Outline each blood parasite and name the species.
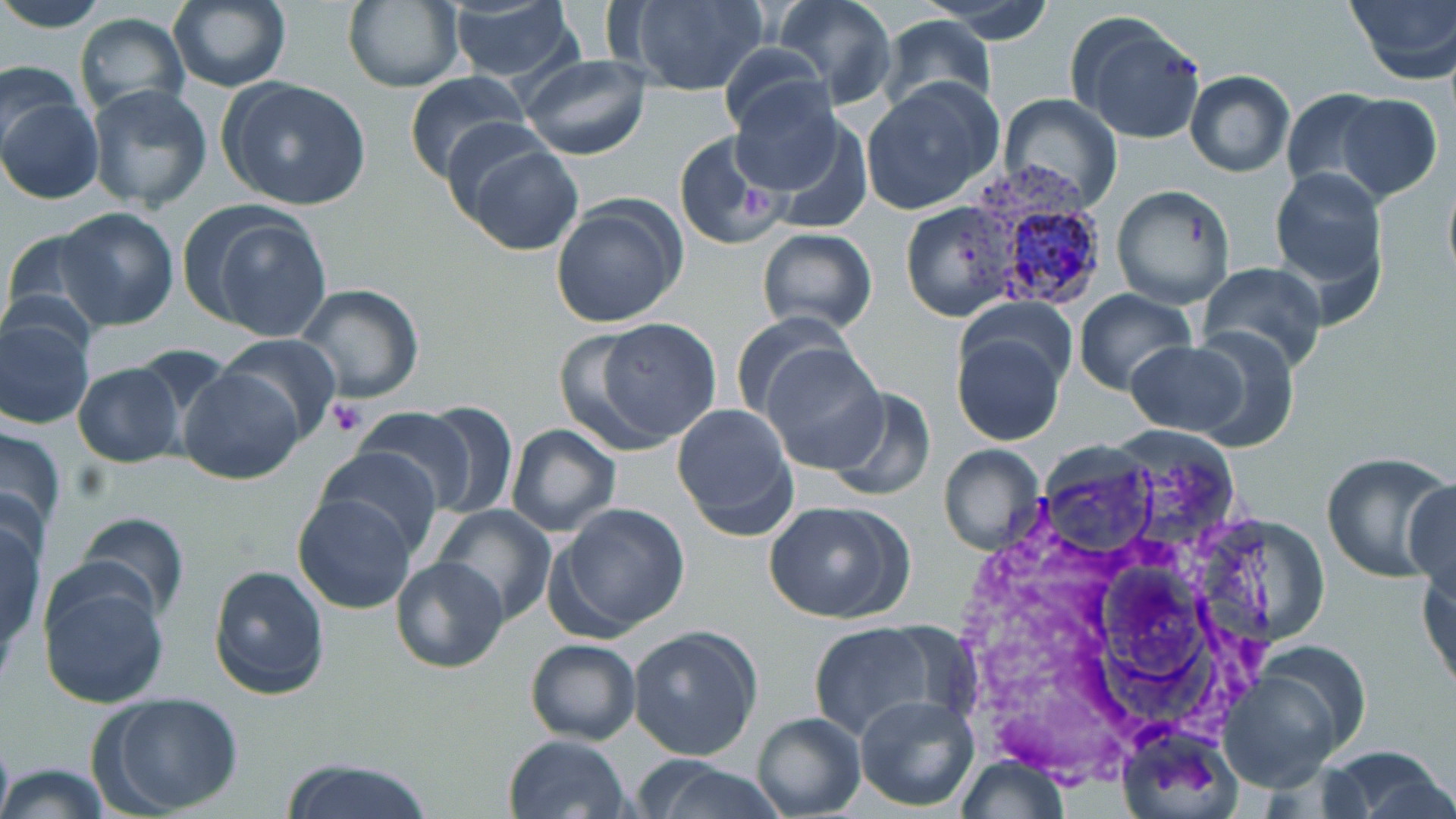
Approximate bounding boxes as named x1/y1/x2/y2 corners in pixels.
Plasmodium vivax-infected red blood cells: (x1=955, y1=162, x2=1109, y2=317).
No Plasmodium falciparum, Plasmodium ovale, Plasmodium malariae, Babesia divergens, or Trypanosoma brucei observed.

slide-level diagnosis = Plasmodium vivax
stain = May-Grünwald-Giemsa
magnification = 1000x
uninfected red blood cell locations = approximate bounding boxes as named x1/y1/x2/y2 corners in pixels: (x1=0, y1=0, x2=110, y2=31), (x1=341, y1=0, x2=465, y2=92), (x1=621, y1=0, x2=768, y2=96), (x1=772, y1=0, x2=896, y2=111), (x1=922, y1=0, x2=1058, y2=44), (x1=1344, y1=0, x2=1456, y2=87), (x1=168, y1=1, x2=290, y2=93), (x1=446, y1=3, x2=582, y2=89), (x1=74, y1=11, x2=190, y2=116), (x1=1068, y1=13, x2=1206, y2=144), (x1=878, y1=14, x2=997, y2=113), (x1=718, y1=40, x2=829, y2=139), (x1=518, y1=53, x2=653, y2=161), (x1=0, y1=61, x2=84, y2=156), (x1=1186, y1=69, x2=1295, y2=177), (x1=403, y1=72, x2=534, y2=186), (x1=220, y1=77, x2=374, y2=213), (x1=864, y1=79, x2=1005, y2=215), (x1=728, y1=80, x2=852, y2=201), (x1=85, y1=83, x2=215, y2=213), (x1=1281, y1=87, x2=1390, y2=194), (x1=998, y1=93, x2=1124, y2=212), (x1=1337, y1=93, x2=1442, y2=202), (x1=2, y1=94, x2=103, y2=206), (x1=675, y1=132, x2=787, y2=253), (x1=458, y1=138, x2=584, y2=257), (x1=1269, y1=167, x2=1388, y2=297), (x1=1441, y1=168, x2=1456, y2=292), (x1=1109, y1=185, x2=1235, y2=309), (x1=551, y1=196, x2=686, y2=329), (x1=899, y1=201, x2=1022, y2=322), (x1=189, y1=205, x2=333, y2=343), (x1=57, y1=206, x2=179, y2=331), (x1=755, y1=227, x2=878, y2=335), (x1=3, y1=228, x2=112, y2=337), (x1=1196, y1=263, x2=1328, y2=376), (x1=293, y1=283, x2=425, y2=404), (x1=1075, y1=289, x2=1198, y2=396), (x1=728, y1=311, x2=856, y2=425), (x1=1, y1=313, x2=95, y2=429), (x1=585, y1=318, x2=724, y2=446), (x1=951, y1=324, x2=1069, y2=447), (x1=1183, y1=328, x2=1301, y2=452), (x1=216, y1=334, x2=343, y2=447), (x1=1123, y1=341, x2=1247, y2=435), (x1=761, y1=343, x2=889, y2=473), (x1=73, y1=363, x2=184, y2=467), (x1=177, y1=364, x2=308, y2=485), (x1=821, y1=386, x2=936, y2=501), (x1=416, y1=401, x2=518, y2=520), (x1=670, y1=401, x2=800, y2=540), (x1=353, y1=405, x2=478, y2=509), (x1=0, y1=423, x2=67, y2=547), (x1=505, y1=423, x2=621, y2=537), (x1=937, y1=444, x2=1046, y2=557), (x1=315, y1=447, x2=445, y2=557), (x1=1320, y1=450, x2=1456, y2=584), (x1=1405, y1=479, x2=1456, y2=604), (x1=292, y1=492, x2=417, y2=613), (x1=764, y1=499, x2=914, y2=625), (x1=549, y1=503, x2=692, y2=638), (x1=434, y1=504, x2=556, y2=622), (x1=0, y1=511, x2=48, y2=663), (x1=76, y1=511, x2=189, y2=623), (x1=1418, y1=552, x2=1456, y2=697), (x1=390, y1=556, x2=508, y2=673), (x1=208, y1=564, x2=331, y2=698), (x1=36, y1=567, x2=169, y2=709), (x1=805, y1=620, x2=954, y2=744), (x1=627, y1=624, x2=763, y2=762), (x1=524, y1=638, x2=640, y2=745), (x1=1218, y1=647, x2=1367, y2=791), (x1=92, y1=690, x2=245, y2=816), (x1=853, y1=694, x2=977, y2=813), (x1=752, y1=710, x2=866, y2=818), (x1=1115, y1=728, x2=1237, y2=817), (x1=502, y1=733, x2=631, y2=818), (x1=1319, y1=746, x2=1456, y2=817), (x1=955, y1=756, x2=1072, y2=817), (x1=277, y1=758, x2=440, y2=819), (x1=634, y1=759, x2=784, y2=819), (x1=0, y1=762, x2=108, y2=818)
field of view = one of a larger specimen
image size = 1456×819 pixels
platelet locations = approximate bounding boxes as named x1/y1/x2/y2 corners in pixels: (x1=327, y1=400, x2=367, y2=436)
modality = light microscopy
preparation = thin blood film